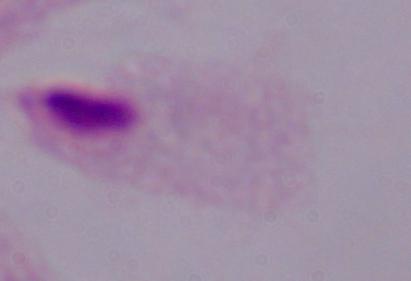
Summary:
  - Identification: trichomonad
  - Modality: photomicrograph
  - Magnification: 1000x